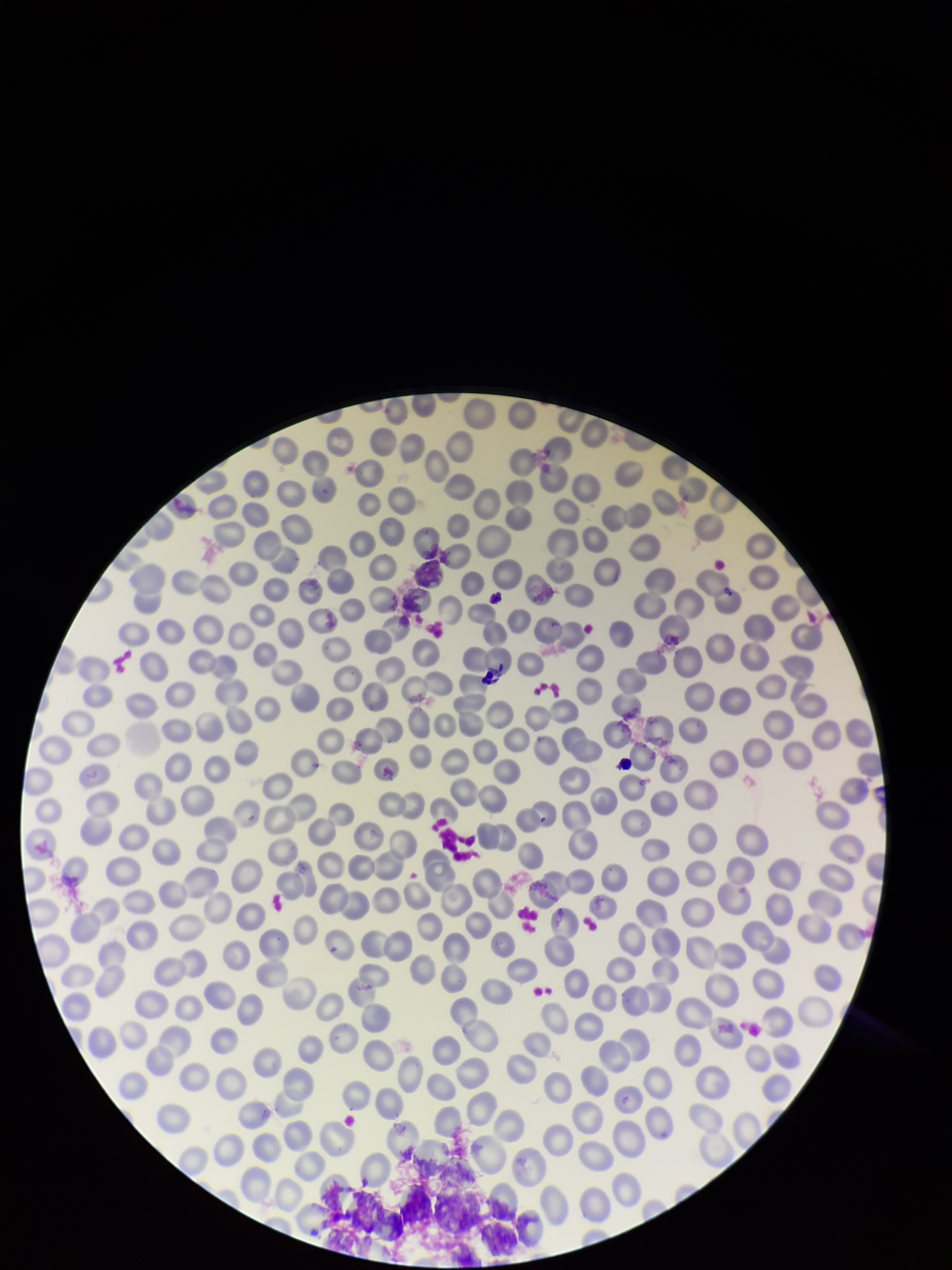
{
  "stain": "Giemsa",
  "red_blood_cell_count": 268,
  "field_of_view": "single",
  "patient_malaria_status": "negative",
  "image_size": "952×1270 pixels",
  "parasitized_red_blood_cells": "none identified",
  "preparation": "thin blood smear",
  "parasitized_red_blood_cell_count": 0,
  "capture": "smartphone photograph through the microscope eyepiece"
}